Identify the cell.
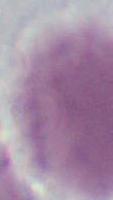
This is an erythrocyte.

Summary:
  - Modality: photomicrograph
  - Magnification: 1000x